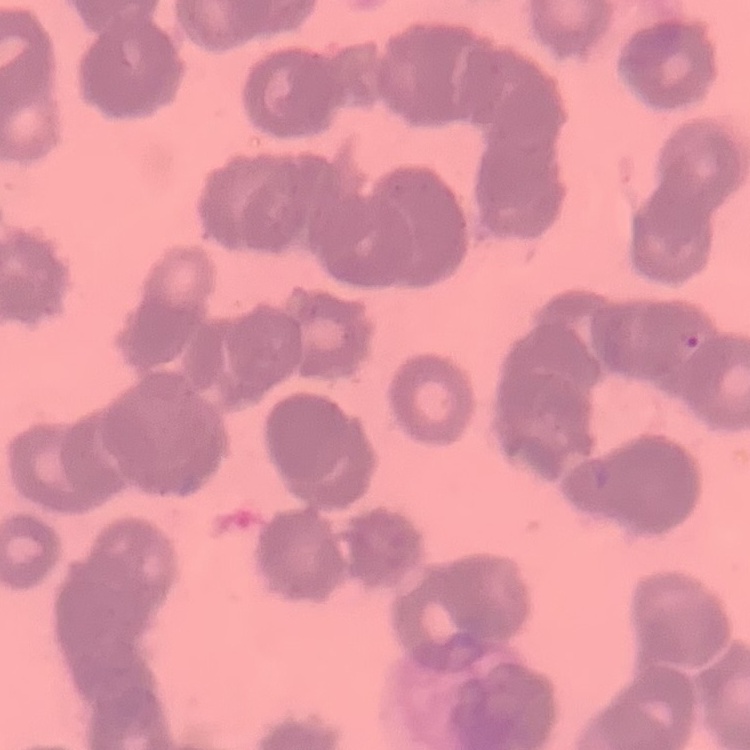
The erythrocytes exhibit rouleaux formation. Field's or Giemsa stain. Thin blood smear. One tile cut from a larger photomicrograph.